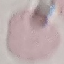

Summary:
  - Malaria status: uninfected
  - Capture: smartphone through the microscope eyepiece
  - Preparation: thin smear
  - Stain: Giemsa
  - Image type: automatically extracted cell patch, resized to 64 × 64 pixels